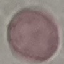

Summary:
  - Malaria status: uninfected
  - Image type: cell patch, automatically extracted from a larger field of view and resized to 64 × 64 pixels
  - Preparation: thin blood smear
  - Stain: Giemsa
  - Capture: smartphone through the microscope eyepiece